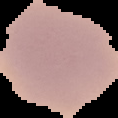

Summary:
  - Preparation: thin blood film
  - Image type: segmented cell region with the area outside set to black
  - Image size: 118×118 pixels
  - Result: no malaria parasites seen